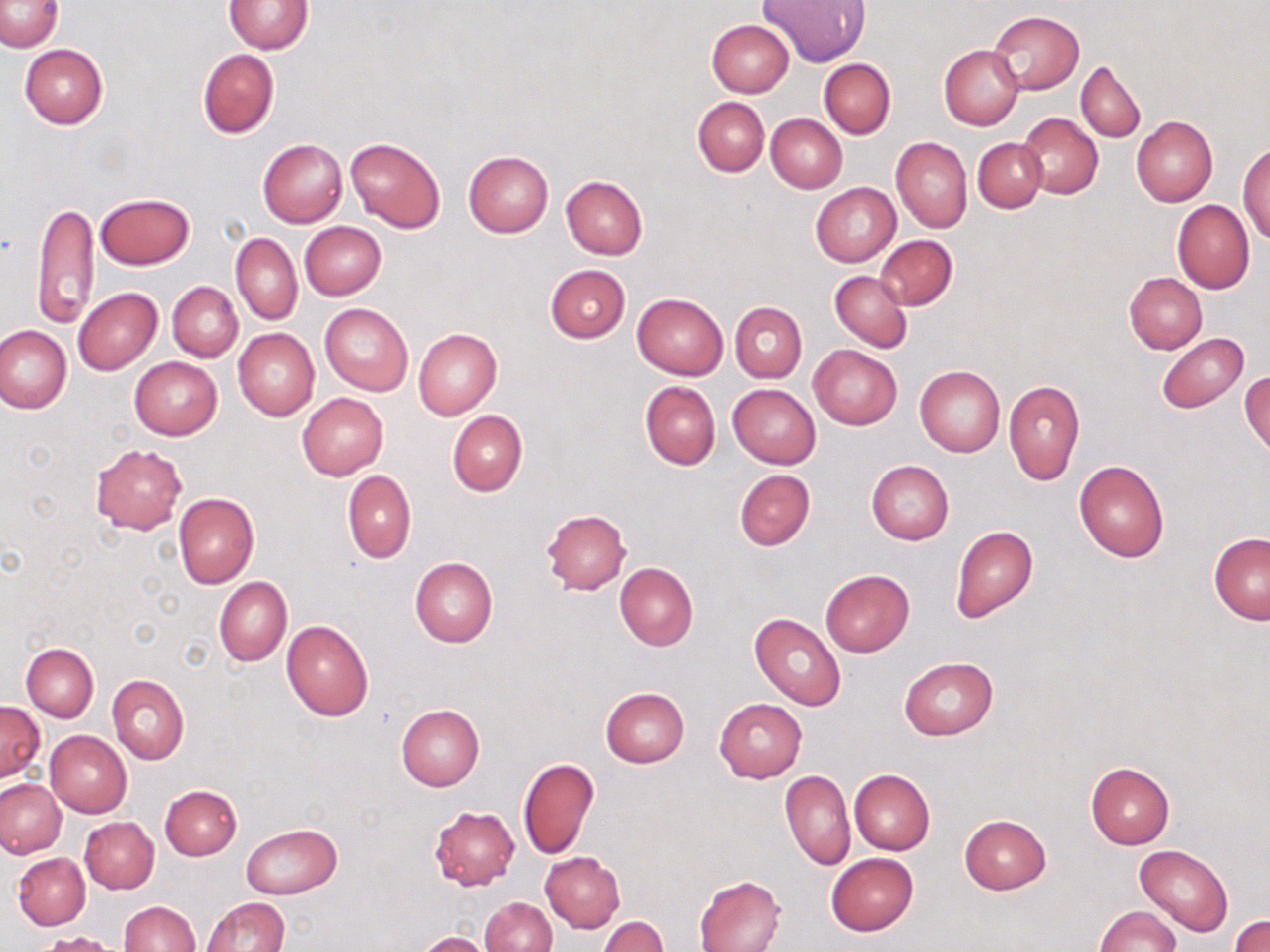
slide-level diagnosis = no evidence of blood parasites
preparation = thin blood film
image size = 1270×952 pixels
magnification = 1000x
stain = May-Grünwald-Giemsa
field of view = one of a larger specimen
uninfected red blood cell locations = approximate bounding boxes as (x1,y1)-(x2,y2) corner pairs in pixels: (761,0)-(870,66), (0,1)-(64,51), (224,1)-(312,54), (988,10)-(1084,94), (707,19)-(794,97), (20,44)-(108,128), (939,46)-(1024,130), (198,49)-(279,138), (820,58)-(895,139), (1076,59)-(1146,142), (692,97)-(769,176), (1017,112)-(1103,198), (766,114)-(846,192), (1131,115)-(1218,207), (891,136)-(972,232), (344,137)-(446,232), (973,137)-(1047,213), (258,139)-(348,228), (1238,142)-(1270,243), (464,150)-(553,237), (561,176)-(648,260), (811,182)-(901,267), (96,193)-(194,269), (33,198)-(99,325), (1172,200)-(1255,293), (300,221)-(387,300), (231,233)-(301,324), (876,235)-(957,310), (833,247)-(949,339), (544,264)-(630,343), (829,271)-(911,353), (1123,272)-(1207,353), (167,282)-(243,362), (74,288)-(163,375), (633,293)-(729,379), (730,302)-(807,382), (320,303)-(413,395), (0,327)-(72,413), (233,328)-(319,420), (413,329)-(501,419), (1156,333)-(1248,413), (808,344)-(902,430), (130,357)-(222,439), (915,366)-(1004,457), (1240,372)-(1269,457), (1003,380)-(1084,486), (639,381)-(721,470), (728,384)-(821,469), (297,393)-(389,480), (447,409)-(528,496), (90,444)-(187,533), (866,460)-(954,545), (1074,460)-(1170,563), (342,469)-(416,563), (734,469)-(815,550), (174,493)-(259,590), (541,509)-(631,595), (950,525)-(1038,623), (1209,532)-(1269,624), (410,557)-(497,648), (615,562)-(697,652), (821,569)-(914,656), (213,577)-(291,667), (750,613)-(846,711), (281,620)-(374,721), (21,643)-(98,721), (899,658)-(997,739), (107,674)-(189,764), (600,687)-(689,767), (714,698)-(807,783), (0,701)-(44,782), (397,705)-(485,791), (45,730)-(132,817), (8,744)-(122,839), (518,758)-(599,860), (1086,762)-(1174,848), (849,769)-(934,855), (780,770)-(855,871), (6,778)-(75,932), (1,779)-(66,857), (160,784)-(242,860), (428,806)-(519,890), (959,814)-(1050,894), (80,817)-(159,893), (241,822)-(342,899), (1134,844)-(1233,937), (540,852)-(625,932), (826,852)-(918,935), (14,853)-(90,929), (695,875)-(787,952), (202,897)-(290,952), (481,897)-(556,952), (120,900)-(201,952), (1094,905)-(1180,952), (1231,913)-(1270,951), (598,917)-(669,952), (414,931)-(490,952)
modality = optical microscopy